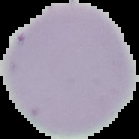
Image is 139×139 pixels. From a thin blood smear. Cell region segmented out of the field of view; the surrounding area is masked to black. Result: negative for malaria parasites.